Report the malaria status of this cell.
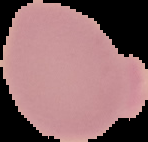

Uninfected.

Summary:
  - Preparation: thin blood film
  - Image type: cell region segmented out of the field of view; surrounding area masked to black
  - Image size: 148×142 pixels